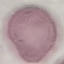

Summary:
  - Malaria status: uninfected
  - Preparation: thin blood film
  - Stain: Giemsa
  - Capture: smartphone camera at the microscope eyepiece
  - Image type: cell patch, automatically extracted from a larger field of view and resized to 64 × 64 pixels